Assess this cell for malaria.
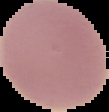

It is uninfected.

Image is 109×112 pixels. The area outside the segmented cell region is set to black. From a thin blood film.